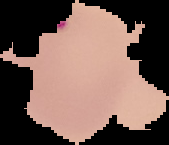

Summary:
  - Image size: 169×145 pixels
  - Preparation: thin blood film
  - Malaria status: parasitized
  - Image type: segmented cell region on a black background